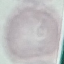 Malaria status: uninfected. Automatically extracted cell patch, resized to 64 × 64 pixels. Acquired by smartphone through the microscope eyepiece. Thin blood smear. Giemsa-stained preparation.